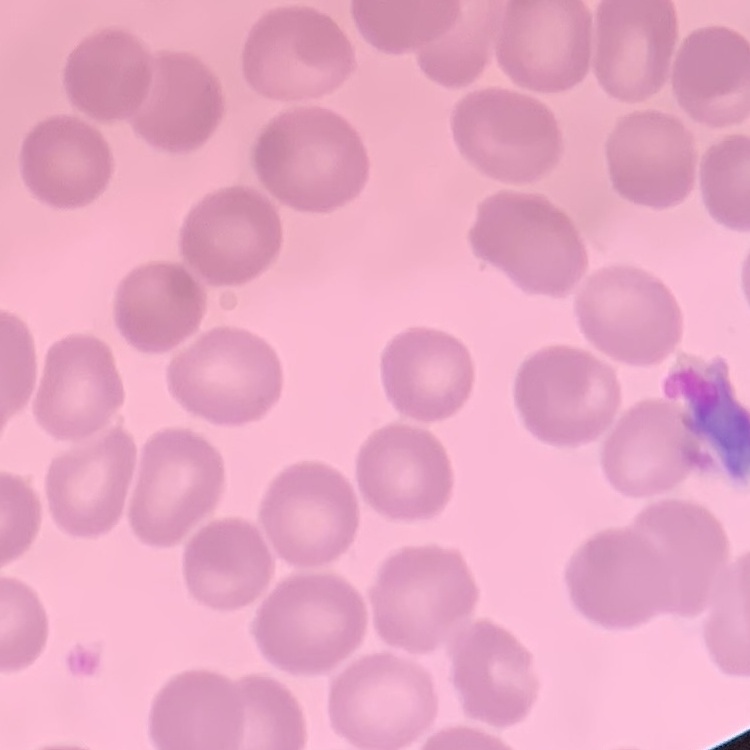
Summary:
  - Erythrocyte morphology: no rouleaux formation
  - Image type: one tile cut from a larger photomicrograph
  - Stain: Field's or Giemsa
  - Preparation: thin blood smear